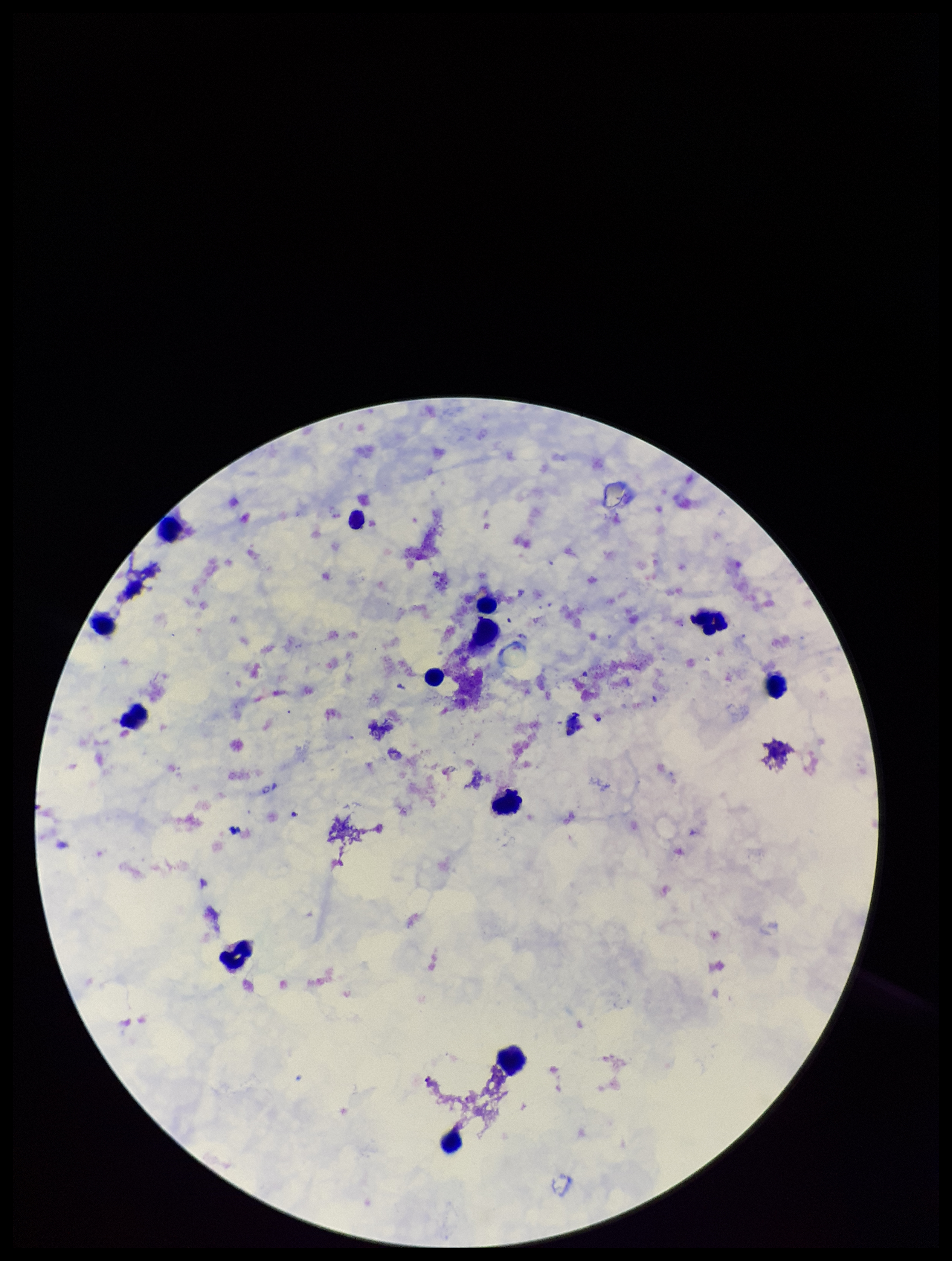
preparation = thick
field of view = single
leukocyte count = 12
image size = 952×1261 pixels
parasite count = 0
capture = smartphone photograph through the microscope eyepiece
stain = Giemsa
patient malaria status = negative
Plasmodium parasites = none seen